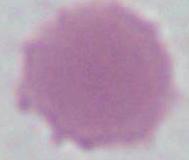

magnification: 1000x
identification: red blood cell
modality: micrograph